Assess the morphology of the red blood cells.
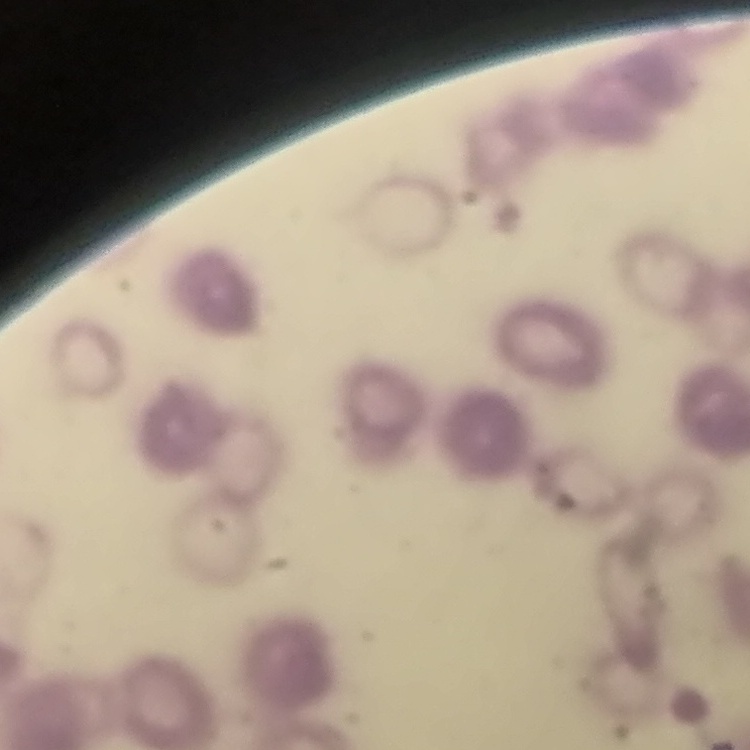
They show rouleaux formation.

Summary:
  - Stain: Field's or Giemsa
  - Image type: square crop of a larger photomicrograph
  - Preparation: thin blood film